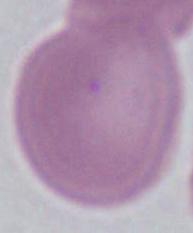

magnification = 1000x
identification = red blood cell
modality = photomicrograph